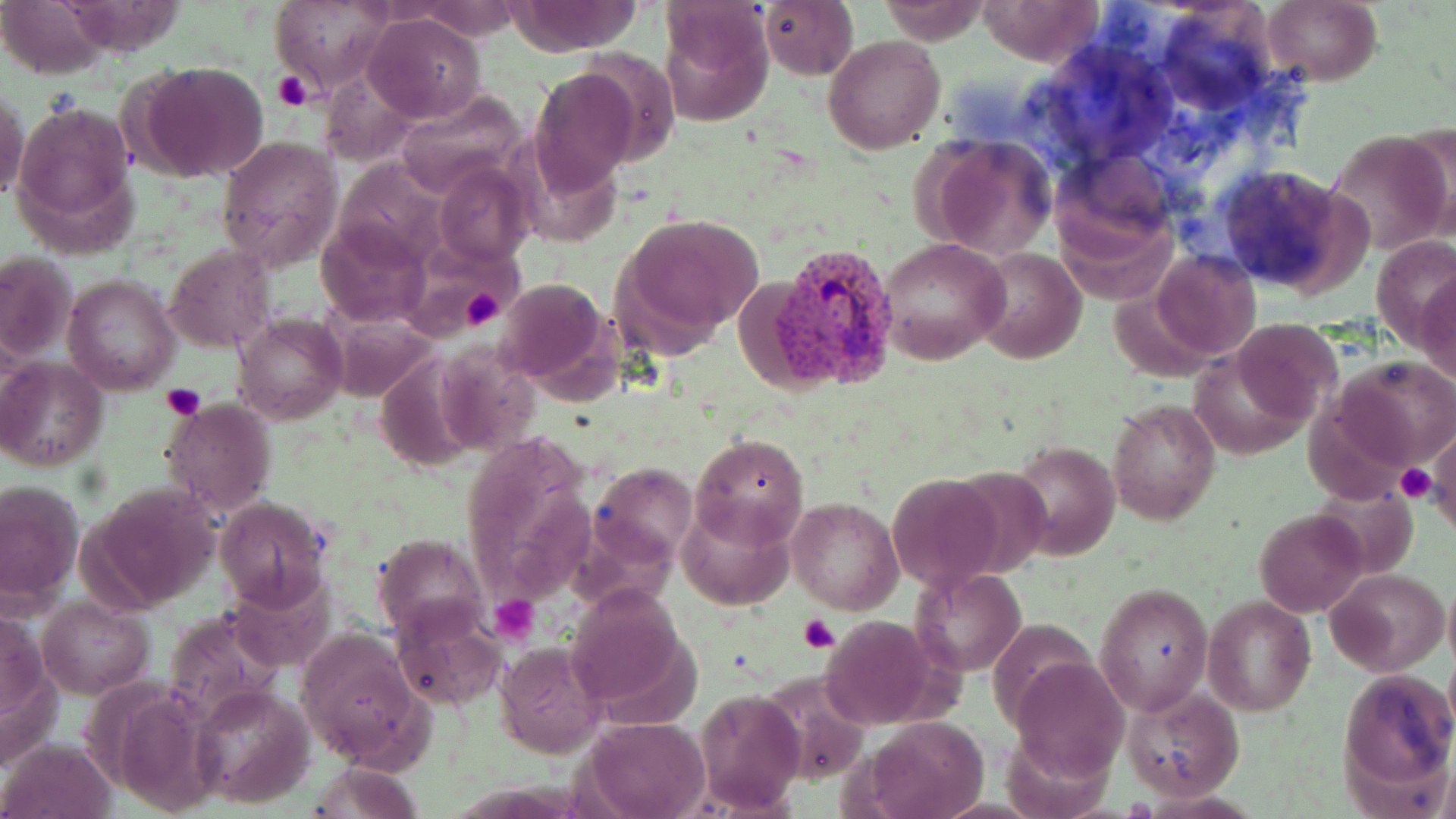
Summary:
  - Coordinate format: approximate bounding boxes as (x1, y1, x2, y2) in pixels
  - Plasmodium vivax-infected red blood cell locations: (752, 242, 901, 390)
  - Uninfected red blood cell locations: (4, 0, 111, 79), (760, 0, 859, 79), (877, 0, 990, 45), (980, 0, 1104, 67), (270, 1, 394, 94), (505, 1, 643, 53), (408, 2, 524, 40), (1261, 2, 1383, 86), (657, 7, 772, 126), (364, 13, 486, 124), (822, 35, 946, 155), (134, 62, 270, 183), (530, 67, 640, 194), (319, 68, 422, 168), (1, 90, 28, 204), (392, 90, 529, 200), (14, 101, 137, 240), (1325, 130, 1454, 256), (919, 134, 1058, 260), (215, 135, 344, 270), (331, 159, 448, 267), (435, 162, 533, 267), (1216, 163, 1365, 297), (623, 212, 765, 340), (316, 220, 429, 326), (878, 236, 1011, 365), (167, 243, 275, 352), (973, 248, 1085, 363), (1148, 250, 1261, 360), (0, 252, 77, 364), (1417, 273, 1456, 383), (62, 274, 180, 395), (494, 277, 615, 393), (330, 312, 439, 402), (235, 314, 345, 425), (1233, 320, 1341, 425), (372, 354, 479, 472), (1333, 356, 1456, 472), (0, 359, 107, 472), (160, 398, 276, 520), (1107, 399, 1221, 525), (458, 434, 599, 613), (692, 435, 807, 549), (1428, 435, 1456, 532), (1008, 438, 1120, 561), (594, 461, 698, 563), (886, 473, 1007, 592), (0, 476, 84, 610), (82, 482, 224, 612), (786, 497, 904, 615), (215, 499, 329, 607), (676, 501, 796, 611), (1255, 508, 1369, 618), (373, 535, 485, 638), (910, 566, 1025, 678), (1330, 568, 1448, 674), (1095, 582, 1215, 717), (1443, 582, 1456, 671), (565, 584, 690, 710), (1205, 596, 1315, 716), (38, 597, 153, 699), (391, 599, 506, 710), (164, 608, 287, 729), (1, 616, 54, 723), (817, 616, 945, 731), (295, 630, 422, 767), (496, 641, 609, 758), (1011, 656, 1128, 782), (1338, 666, 1455, 798), (191, 684, 315, 808), (1123, 686, 1243, 802), (696, 689, 806, 812), (860, 715, 989, 819), (582, 718, 710, 819), (2, 740, 114, 818), (308, 761, 424, 819)
  - Platelet locations: (274, 73, 312, 111), (460, 291, 505, 331), (162, 384, 206, 421), (1397, 462, 1435, 503), (492, 597, 540, 645), (796, 613, 840, 654)
  - Slide-level diagnosis: Plasmodium vivax
  - Field of view: single
  - Preparation: thin blood smear
  - Modality: light microscopy
  - Stain: May-Grünwald-Giemsa
  - Image size: 1456×819 pixels
  - Magnification: 1000x